Name the parasite shown.
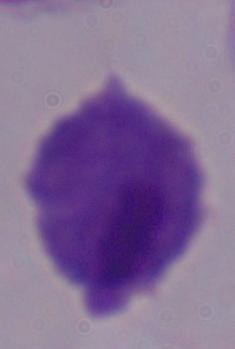
A trichomonad.

modality = micrograph
magnification = 1000x